Identify the cell.
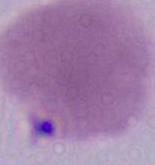
An erythrocyte.

Summary:
  - Magnification: 1000x
  - Modality: micrograph